Name the blood parasite species.
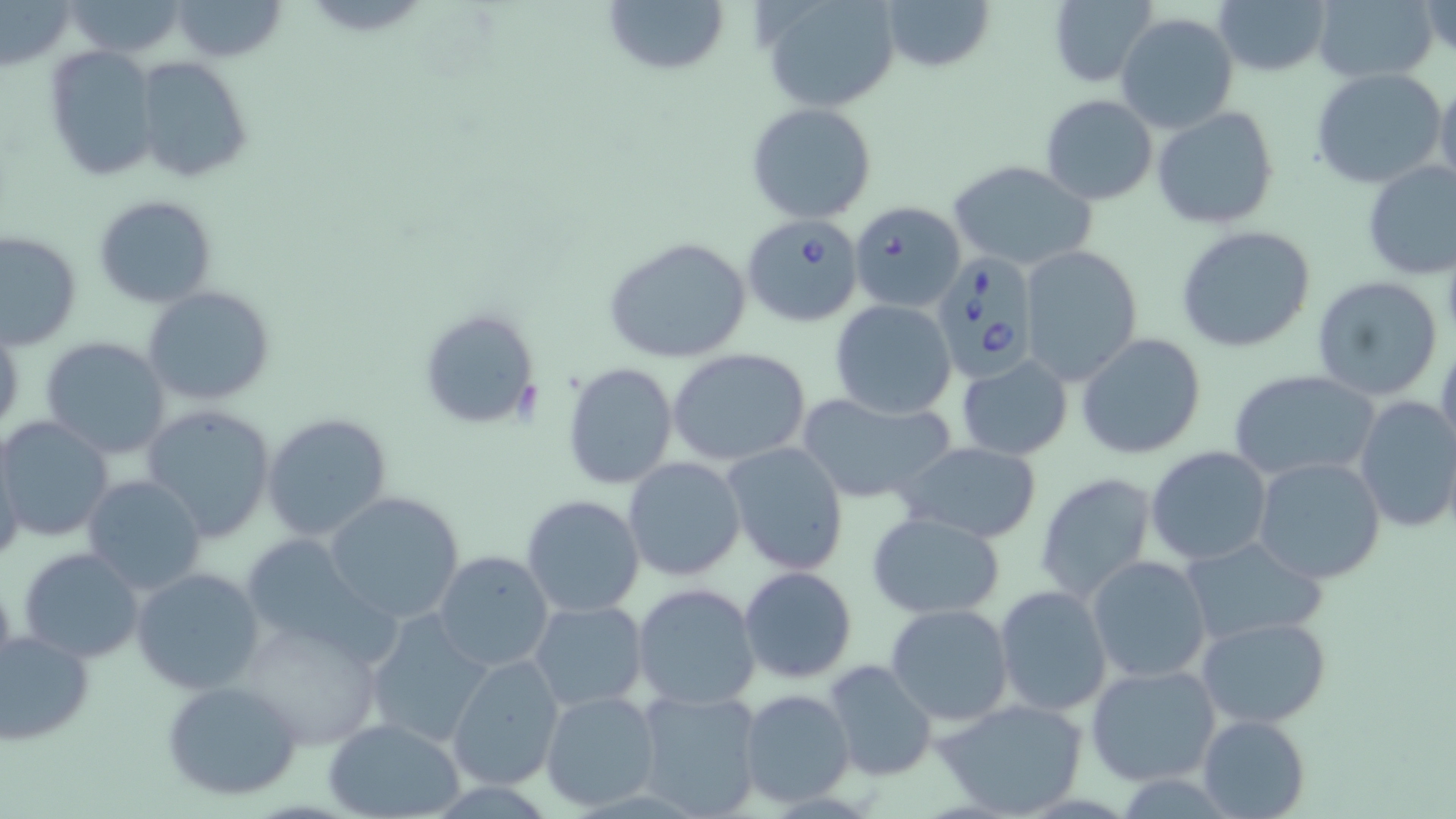
Babesia divergens.

Approximate bounding boxes as named x1/y1/x2/y2 corners in pixels. Babesia divergens-infected red blood cell locations: (x1=847, y1=199, x2=967, y2=314), (x1=743, y1=213, x2=865, y2=328), (x1=930, y1=251, x2=1041, y2=378). Uninfected red blood cell locations: (x1=62, y1=0, x2=192, y2=58), (x1=170, y1=0, x2=287, y2=63), (x1=601, y1=0, x2=730, y2=77), (x1=877, y1=0, x2=995, y2=74), (x1=1046, y1=0, x2=1157, y2=88), (x1=1210, y1=0, x2=1333, y2=77), (x1=1310, y1=0, x2=1440, y2=84), (x1=1421, y1=0, x2=1455, y2=62), (x1=1, y1=1, x2=76, y2=70), (x1=761, y1=1, x2=902, y2=111), (x1=1117, y1=11, x2=1239, y2=134), (x1=43, y1=45, x2=157, y2=180), (x1=137, y1=57, x2=253, y2=184), (x1=1310, y1=68, x2=1448, y2=190), (x1=1434, y1=74, x2=1456, y2=192), (x1=1040, y1=94, x2=1158, y2=205), (x1=746, y1=102, x2=878, y2=223), (x1=1151, y1=104, x2=1280, y2=229), (x1=946, y1=158, x2=1098, y2=272), (x1=1360, y1=159, x2=1456, y2=278), (x1=93, y1=195, x2=219, y2=308), (x1=1175, y1=225, x2=1317, y2=353), (x1=1, y1=231, x2=81, y2=350), (x1=603, y1=235, x2=753, y2=364), (x1=1018, y1=244, x2=1144, y2=384), (x1=1310, y1=275, x2=1444, y2=401), (x1=144, y1=287, x2=275, y2=406), (x1=830, y1=300, x2=957, y2=419), (x1=417, y1=306, x2=542, y2=431), (x1=1077, y1=333, x2=1207, y2=460), (x1=40, y1=336, x2=171, y2=459), (x1=1435, y1=345, x2=1456, y2=468), (x1=666, y1=348, x2=813, y2=466), (x1=955, y1=354, x2=1073, y2=461), (x1=561, y1=362, x2=679, y2=489), (x1=1229, y1=370, x2=1381, y2=484), (x1=797, y1=391, x2=957, y2=506), (x1=1353, y1=396, x2=1456, y2=532), (x1=141, y1=405, x2=275, y2=542), (x1=262, y1=412, x2=393, y2=544), (x1=0, y1=418, x2=112, y2=543), (x1=723, y1=442, x2=849, y2=575), (x1=898, y1=442, x2=1043, y2=543), (x1=0, y1=444, x2=25, y2=572), (x1=1146, y1=446, x2=1273, y2=565), (x1=622, y1=455, x2=746, y2=581), (x1=1251, y1=455, x2=1389, y2=586), (x1=1035, y1=471, x2=1157, y2=604), (x1=81, y1=475, x2=207, y2=595), (x1=323, y1=490, x2=465, y2=624), (x1=1057, y1=492, x2=1181, y2=671), (x1=522, y1=494, x2=645, y2=616), (x1=866, y1=510, x2=1006, y2=619), (x1=237, y1=534, x2=386, y2=659), (x1=1181, y1=535, x2=1326, y2=646), (x1=873, y1=539, x2=1018, y2=680), (x1=18, y1=547, x2=144, y2=663), (x1=432, y1=550, x2=554, y2=672), (x1=1087, y1=555, x2=1215, y2=684), (x1=132, y1=565, x2=266, y2=694), (x1=738, y1=565, x2=857, y2=684), (x1=0, y1=572, x2=19, y2=693), (x1=632, y1=581, x2=762, y2=709), (x1=993, y1=584, x2=1112, y2=717), (x1=529, y1=599, x2=649, y2=712), (x1=884, y1=602, x2=1014, y2=725), (x1=361, y1=611, x2=492, y2=750), (x1=1197, y1=615, x2=1331, y2=728), (x1=238, y1=616, x2=382, y2=747), (x1=0, y1=630, x2=96, y2=746), (x1=444, y1=653, x2=565, y2=791), (x1=824, y1=660, x2=938, y2=780), (x1=1084, y1=662, x2=1224, y2=786), (x1=162, y1=680, x2=304, y2=801), (x1=631, y1=686, x2=764, y2=817), (x1=738, y1=689, x2=855, y2=808), (x1=540, y1=690, x2=662, y2=811), (x1=934, y1=697, x2=1090, y2=819), (x1=1197, y1=714, x2=1309, y2=819), (x1=322, y1=717, x2=467, y2=819). 1000x magnification. Light microscopy. Image is 1456×819 pixels. May-Grünwald-Giemsa stain. One field of a larger specimen. Thin blood smear.